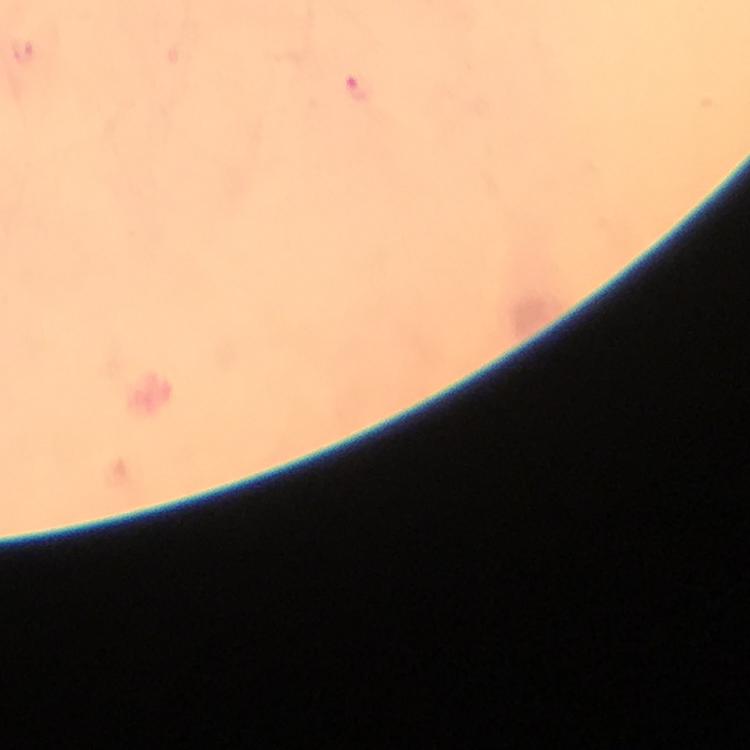
Approximate centers as [x, y] in pixels.
Summary:
  - Malaria parasite locations: [358, 89]
  - Cropped from: one field of view
  - Magnification: 100x
  - Preparation: thick blood film
  - Capture: smartphone mounted on the microscope
  - Immersion oil: applied
  - Context: from a diagnostic examination for malaria
  - Stain: Giemsa
  - Image size: 750×750 pixels